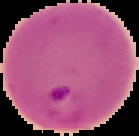
image_size: 139×136 pixels
image_type: segmented cell region with the area outside set to black
preparation: thin blood smear
result: malaria parasites detected